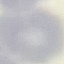

Result: no malaria parasites detected. Acquired by smartphone through the microscope eyepiece. Automatically extracted cell patch, resized to 64 × 64 pixels. Thin smear of blood. Giemsa-stained preparation.